Assess the morphology of the erythrocytes.
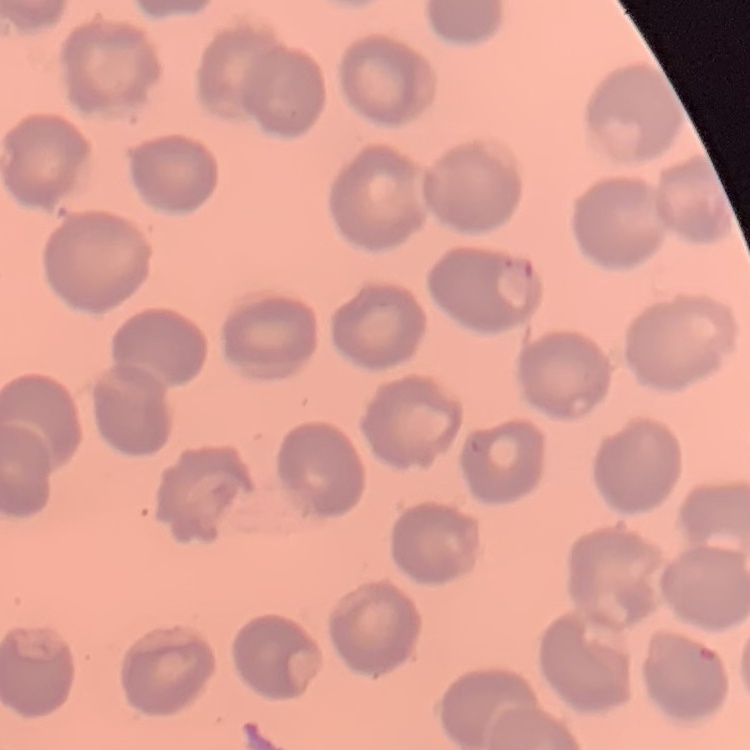
No rouleaux formation.

image_type: square crop of a larger photomicrograph
preparation: thin peripheral smear
stain: Field's or Giemsa